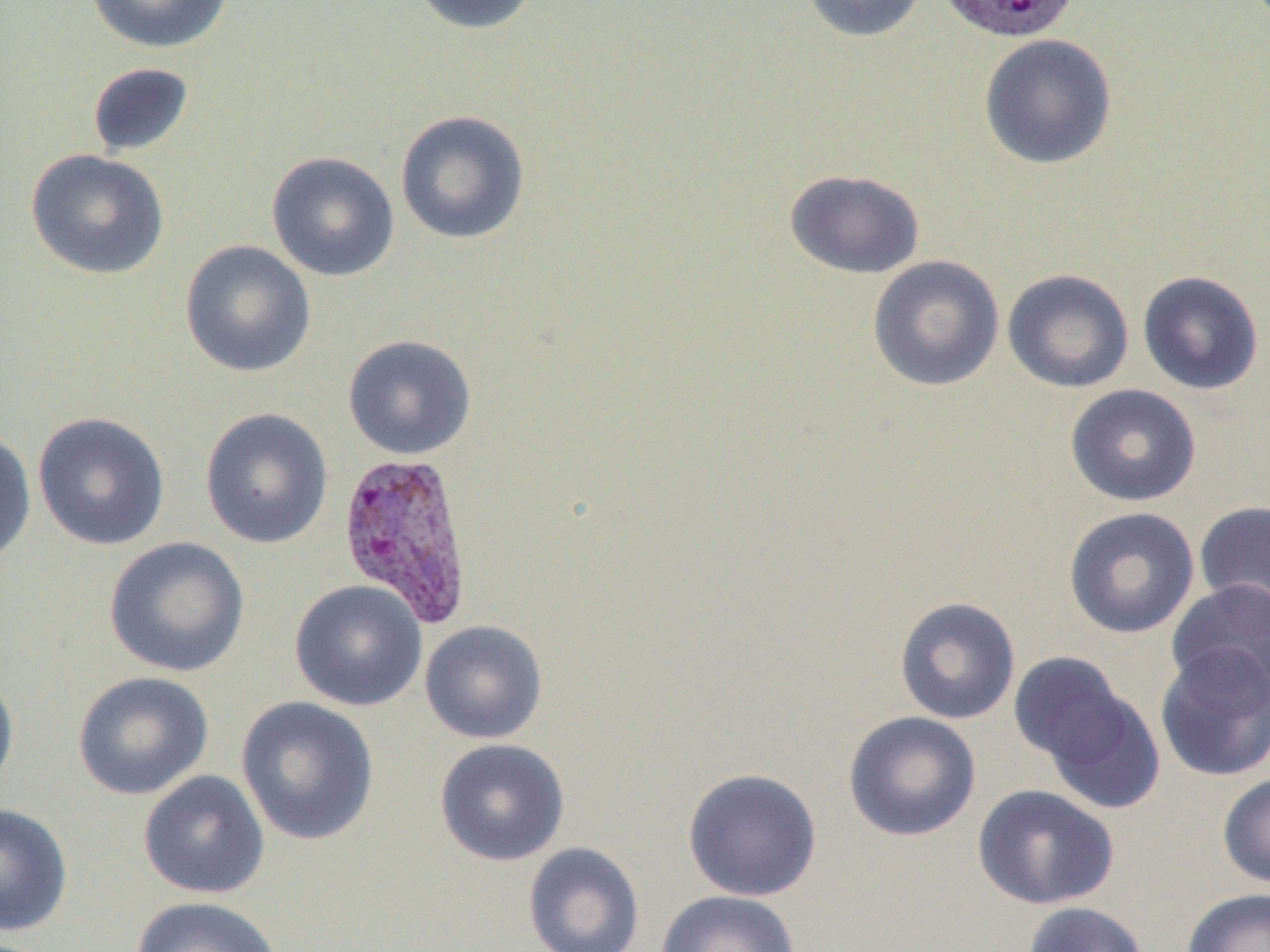

slide_level_diagnosis: Plasmodium vivax
modality: optical microscopy
preparation: thin blood smear
uninfected_red_blood_cell_locations: 'approximate bounding boxes as [x1, y1, x2, y2] in pixels: [85, 0, 234, 54], [409, 0, 541, 35], [800, 0, 929, 43], [978, 33, 1118, 170], [87, 62, 195, 157], [394, 109, 532, 245], [26, 149, 171, 280], [266, 151, 401, 282], [783, 169, 926, 279], [180, 239, 317, 378], [867, 255, 1005, 392], [1002, 268, 1134, 393], [1137, 270, 1265, 396], [342, 334, 477, 461], [1065, 384, 1202, 506], [199, 407, 334, 549], [32, 411, 171, 550], [0, 428, 36, 569], [1193, 500, 1270, 623], [1062, 506, 1200, 639], [103, 536, 251, 678], [289, 579, 428, 712], [1166, 579, 1270, 703], [893, 596, 1021, 725], [419, 619, 548, 744], [1154, 643, 1270, 783], [1007, 651, 1134, 771], [0, 668, 20, 800], [72, 671, 214, 801], [1035, 681, 1166, 815], [236, 696, 380, 846], [843, 711, 981, 842], [434, 738, 571, 866], [682, 767, 822, 902], [138, 770, 271, 899], [1217, 772, 1270, 888], [972, 784, 1119, 910], [0, 803, 73, 936], [523, 842, 646, 952], [1181, 888, 1270, 952], [655, 890, 801, 952], [130, 895, 284, 952], [1021, 901, 1150, 952]'
magnification: 1000x
plasmodium_vivax_infected_red_blood_cell_locations: 'approximate bounding boxes as [x1, y1, x2, y2] in pixels: [940, 2, 1087, 40], [336, 451, 475, 627]'
image_size: 1270×952 pixels
field_of_view: single